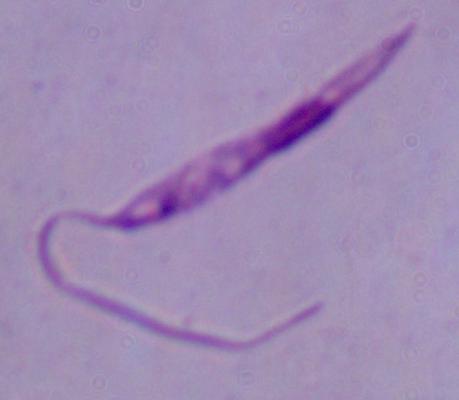
Micrograph. 1000x magnification. A Leishmania parasite is seen.